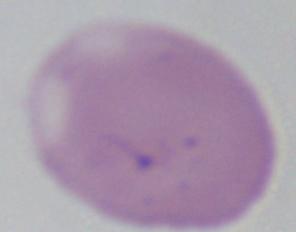

A Babesia parasite is shown. 1000x magnification. Photomicrograph.